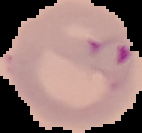

Summary:
  - Result: malaria parasites identified
  - Preparation: thin blood film
  - Image type: cell region segmented out of the field of view; surrounding area masked to black
  - Image size: 142×133 pixels